State which parasite is depicted.
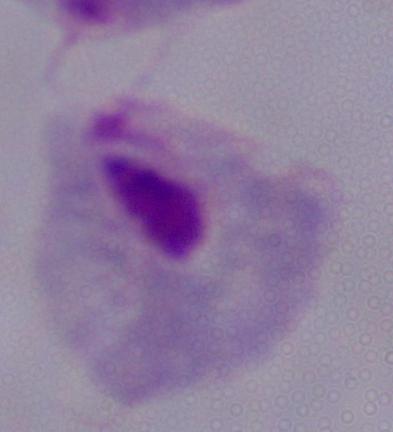
This is a trichomonad.

1000x magnification. Photomicrograph.